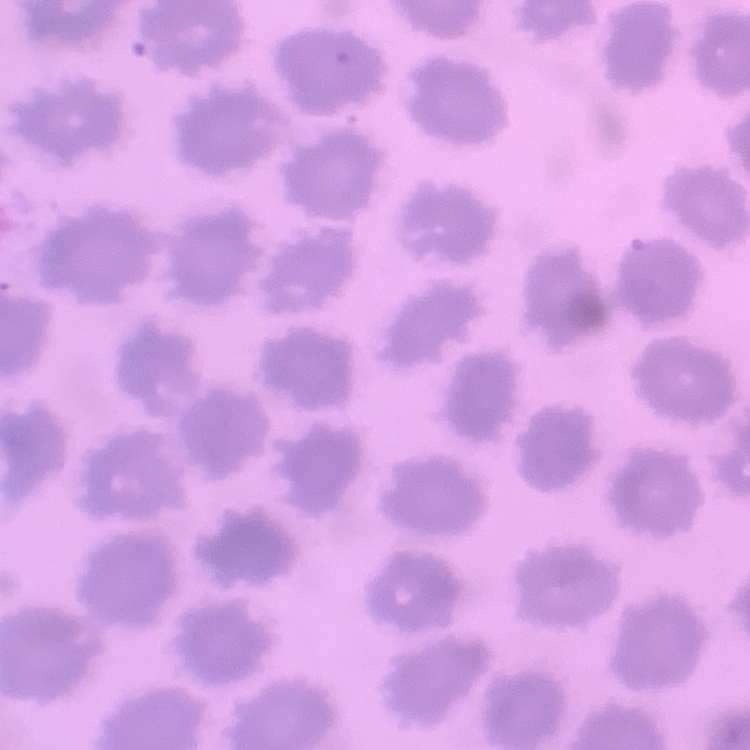 The erythrocytes exhibit no rouleaux formation. Field's or Giemsa stain. Thin peripheral smear. Square crop of a larger photomicrograph.